Comment on the morphology of the red blood cells.
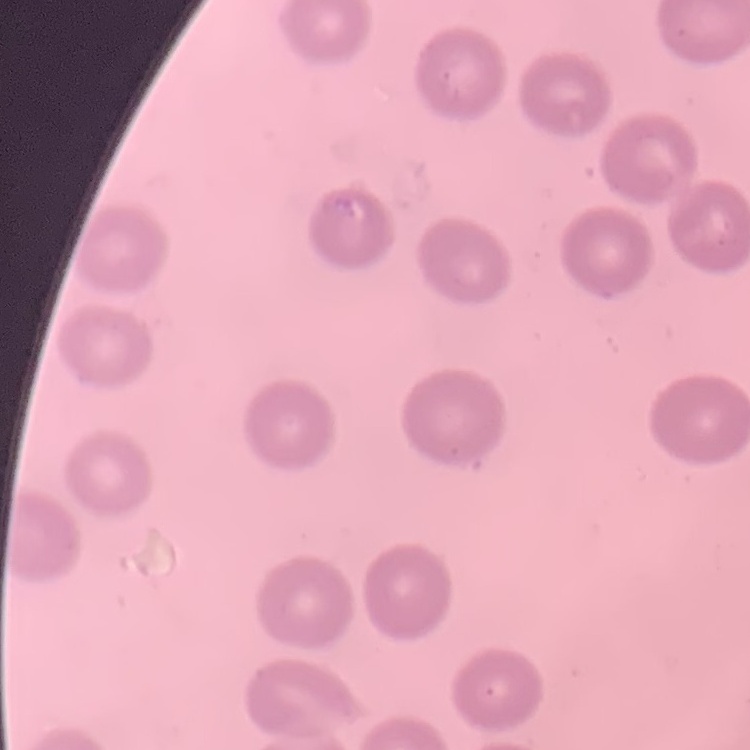
No rouleaux formation.

Stained with either Field's or Giemsa. Thin blood film. Square crop of a larger photomicrograph.